Give the preparation type.
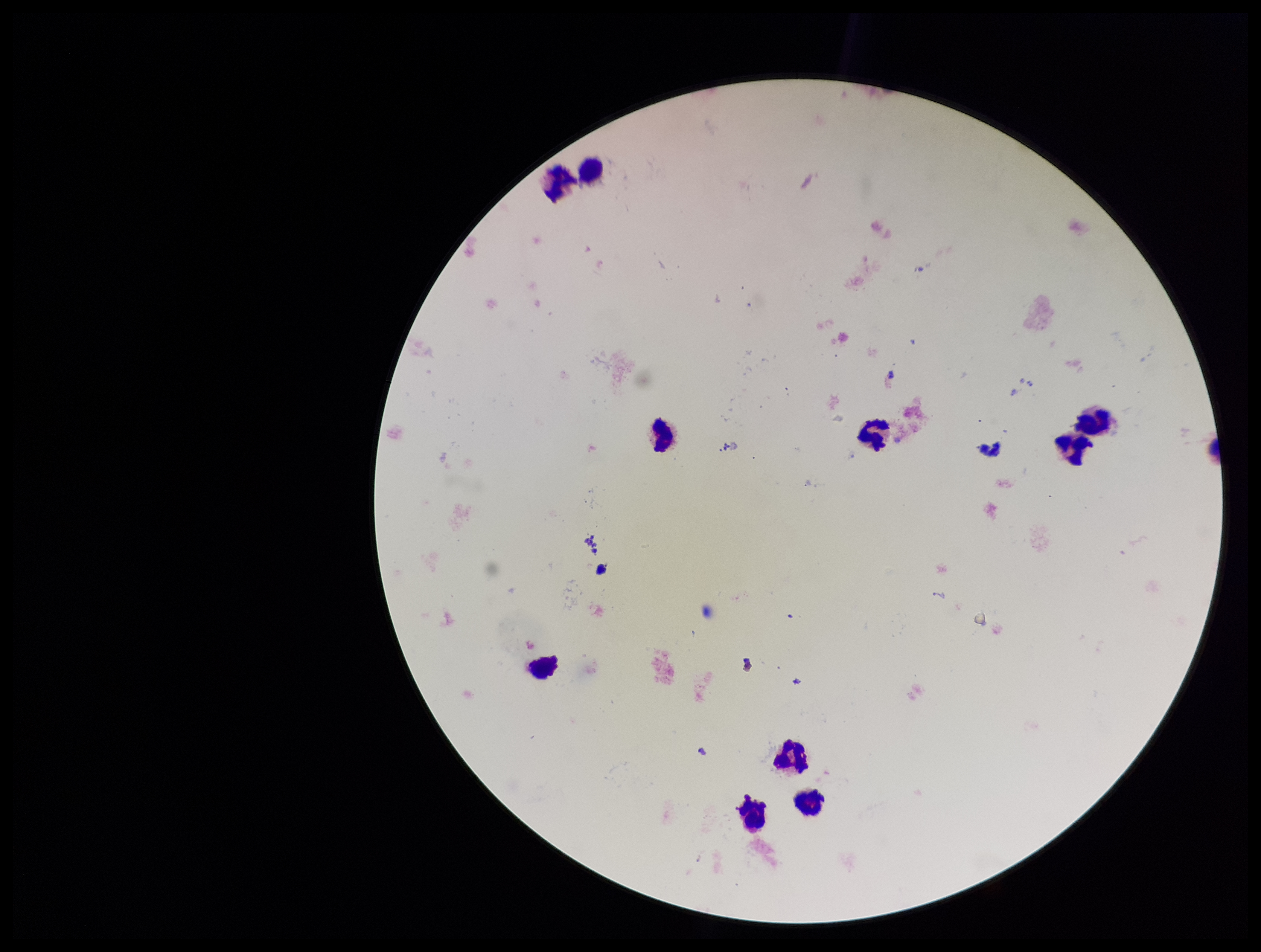
A thick smear.

Summary:
  - Capture: smartphone photograph through the microscope eyepiece
  - Field of view: single
  - Plasmodium parasites: none seen
  - Patient malaria status: negative
  - Stain: Giemsa
  - Leukocyte count: 10
  - Image size: 1261×952 pixels
  - Parasite count: 0